Report the malaria status of this cell.
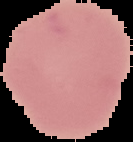
Uninfected.

image type = segmented cell region with the area outside set to black
image size = 133×142 pixels
preparation = thin blood smear